Evaluate for Plasmodium parasites.
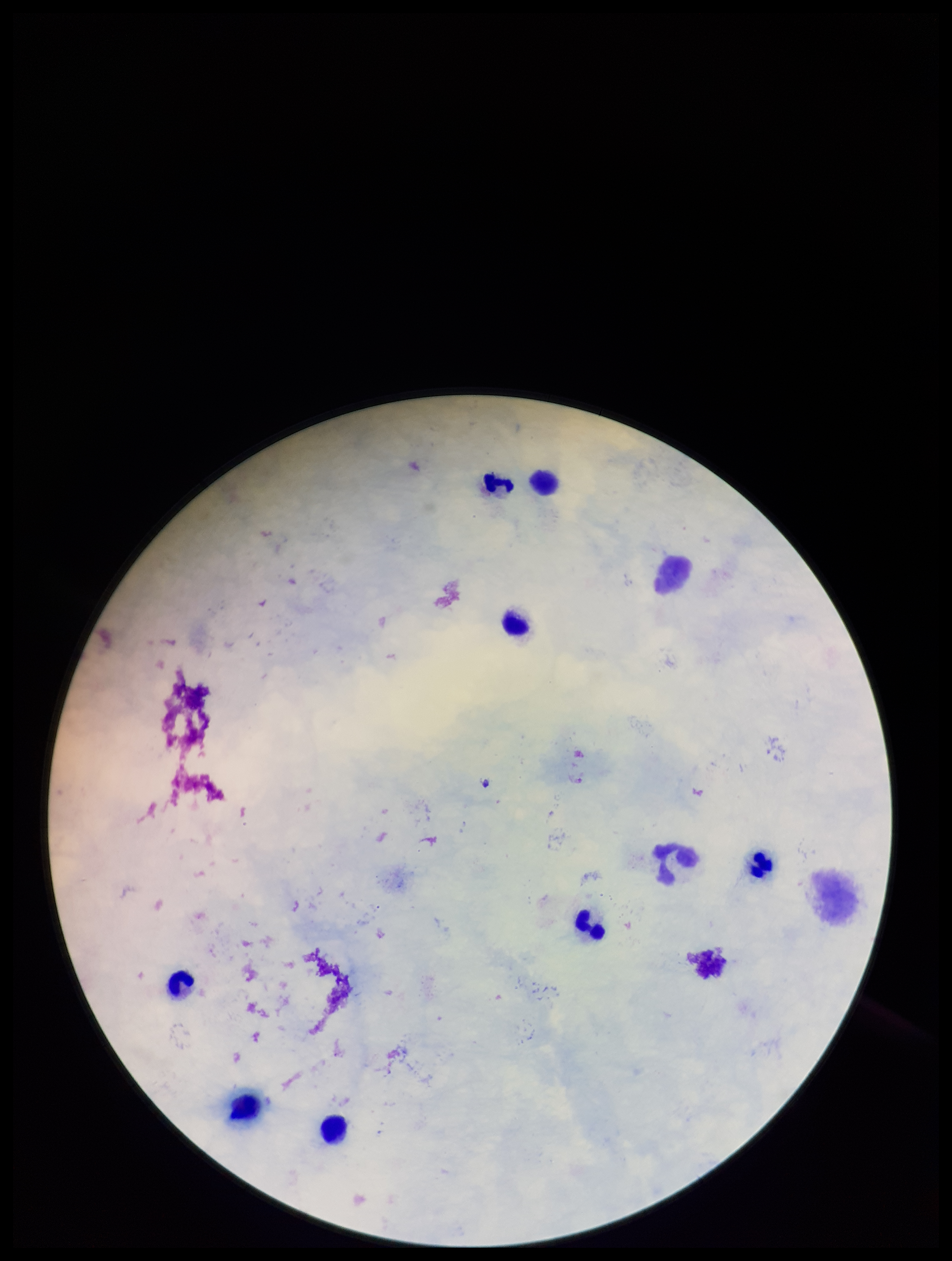

None seen.

Parasite count: 0. Leukocyte count: 9. Photographed through the microscope eyepiece with a smartphone camera. Preparation: thick blood smear. Single field of view. Stained with Giemsa. Patient malaria status: negative. Image is 952×1261 pixels.